Report the malaria status of this cell.
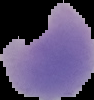

It is parasitized.

Segmented cell region on a black background. From a thin blood film. Image is 94×100 pixels.